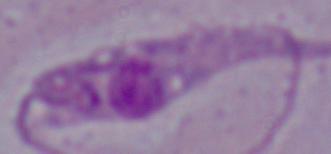
identification = Leishmania
magnification = 1000x
modality = photomicrograph